Locate every Plasmodium falciparum-infected red blood cell.
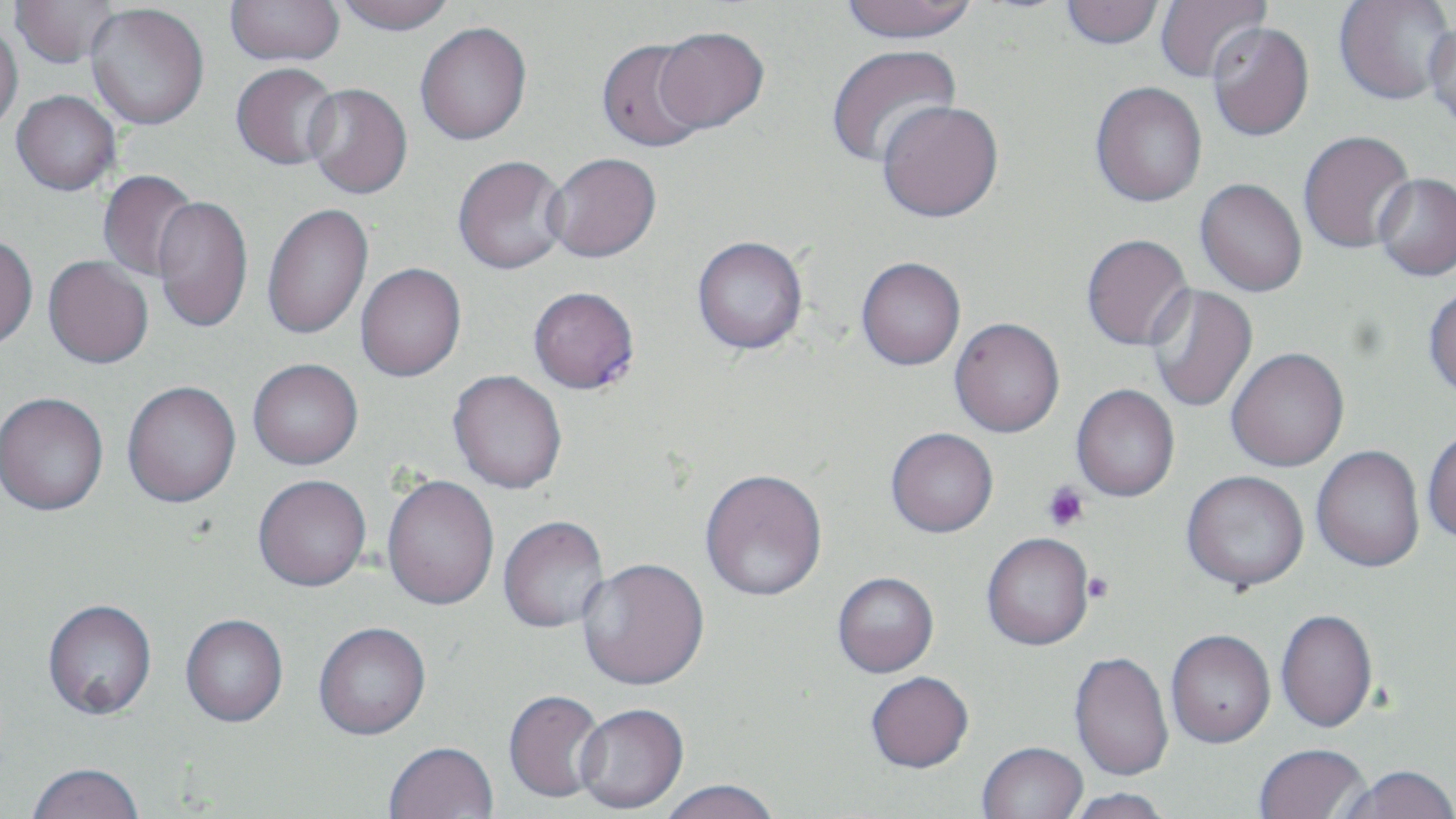
Approximate bounding boxes as (x1, y1, x2, y2) in pixels.
Plasmodium falciparum-infected red blood cells: (528, 286, 639, 395).

Platelet locations: (1041, 481, 1090, 532), (1082, 571, 1113, 603). Uninfected red blood cell locations: (9, 0, 121, 68), (333, 0, 457, 35), (841, 0, 978, 44), (1061, 0, 1165, 49), (1154, 0, 1272, 83), (1334, 0, 1454, 105), (224, 1, 345, 66), (86, 4, 209, 130), (0, 19, 24, 133), (1424, 20, 1456, 133), (415, 22, 532, 145), (1207, 22, 1315, 141), (653, 26, 770, 133), (595, 39, 711, 152), (825, 44, 962, 169), (231, 63, 341, 170), (1090, 81, 1207, 207), (302, 83, 413, 199), (11, 90, 120, 195), (876, 99, 1004, 223), (1298, 130, 1415, 254), (544, 152, 662, 263), (452, 155, 571, 276), (98, 169, 199, 282), (1373, 173, 1456, 281), (1195, 178, 1307, 297), (153, 196, 253, 334), (262, 202, 373, 340), (1081, 233, 1193, 351), (0, 234, 38, 351), (692, 235, 809, 354), (43, 256, 153, 369), (855, 257, 966, 371), (355, 263, 466, 382), (1146, 284, 1258, 413), (1424, 284, 1456, 399), (949, 318, 1065, 439), (1225, 348, 1350, 472), (248, 358, 363, 470), (447, 371, 568, 496), (122, 381, 241, 509), (1070, 385, 1179, 503), (0, 393, 109, 517), (1422, 427, 1456, 545), (885, 431, 998, 540), (1312, 445, 1425, 573), (1182, 470, 1310, 594), (700, 472, 828, 604), (253, 477, 371, 594), (382, 477, 499, 612), (498, 517, 609, 635), (982, 536, 1095, 653), (577, 561, 710, 694), (833, 574, 939, 680), (42, 602, 158, 723), (1276, 609, 1378, 733), (180, 617, 288, 730), (313, 625, 432, 743), (1166, 632, 1276, 751), (1068, 652, 1174, 783), (866, 674, 974, 776), (503, 692, 607, 805), (574, 706, 688, 816), (384, 744, 499, 819), (977, 745, 1088, 819), (1254, 746, 1373, 819), (26, 766, 145, 819), (1338, 768, 1456, 819), (660, 781, 782, 819), (1063, 789, 1172, 819). Slide-level diagnosis: Plasmodium falciparum. Captured at 1000x magnification. May-Grünwald-Giemsa-stained preparation. Single field of view. Light microscopy. Image is 1456×819 pixels. Thin blood smear.